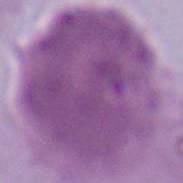

{
  "magnification": "1000x",
  "modality": "photomicrograph",
  "identification": "erythrocyte"
}